Assess the morphology of the red blood cells.
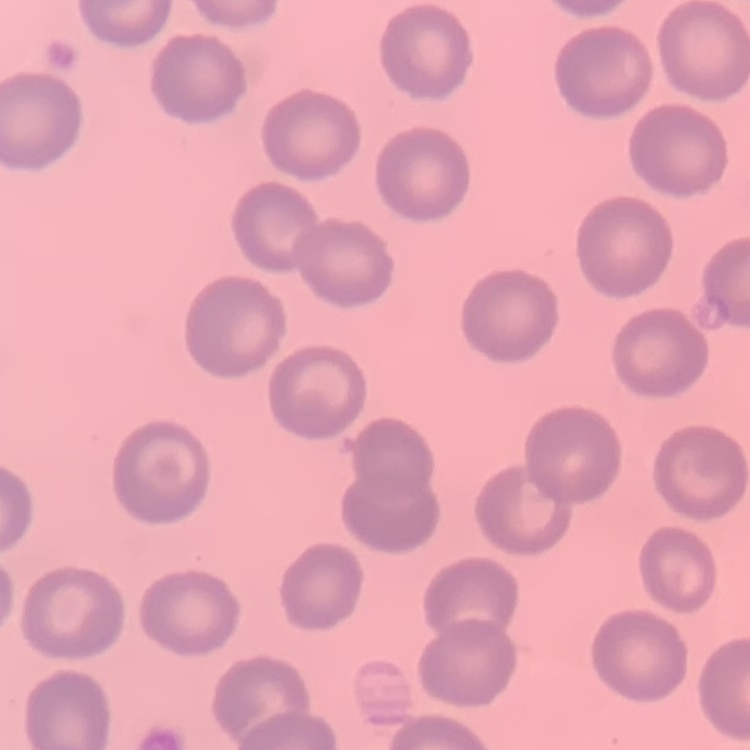

No rouleaux formation.

Field's or Giemsa stain. One tile cut from a larger photomicrograph. Thin blood smear.